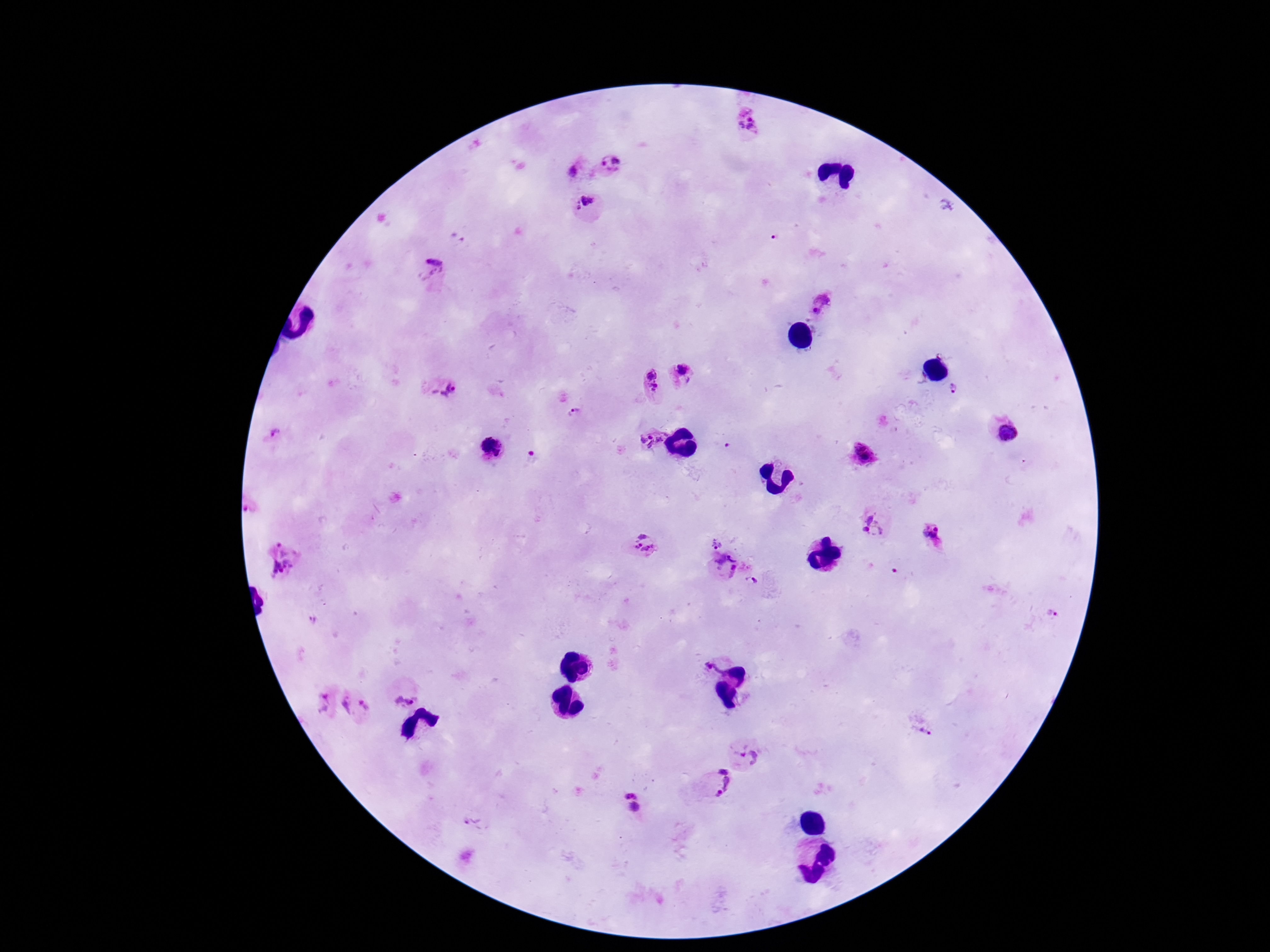 Approximate object centers, in pixels from the top-left corner. Plasmodium parasite locations: (x=750, y=128), (x=612, y=163), (x=573, y=172), (x=584, y=204), (x=456, y=239), (x=432, y=271), (x=822, y=305), (x=683, y=374), (x=652, y=383), (x=954, y=388), (x=445, y=391), (x=574, y=412), (x=275, y=434), (x=1010, y=434), (x=653, y=440), (x=487, y=442), (x=501, y=443), (x=728, y=445), (x=864, y=452), (x=496, y=454), (x=249, y=509), (x=874, y=526), (x=937, y=529), (x=932, y=536), (x=717, y=543), (x=642, y=544), (x=732, y=557), (x=282, y=560), (x=732, y=570), (x=751, y=581), (x=1050, y=615), (x=312, y=621), (x=714, y=669), (x=405, y=696), (x=321, y=703), (x=347, y=705), (x=368, y=706), (x=924, y=733), (x=747, y=755), (x=719, y=783), (x=630, y=793), (x=634, y=806), (x=472, y=823). Single field of view. Image is 1270×952 pixels. Patient malaria status: infected. 100x magnification. Giemsa-stained preparation. Smartphone photograph taken through the microscope eyepiece. Thick blood smear.